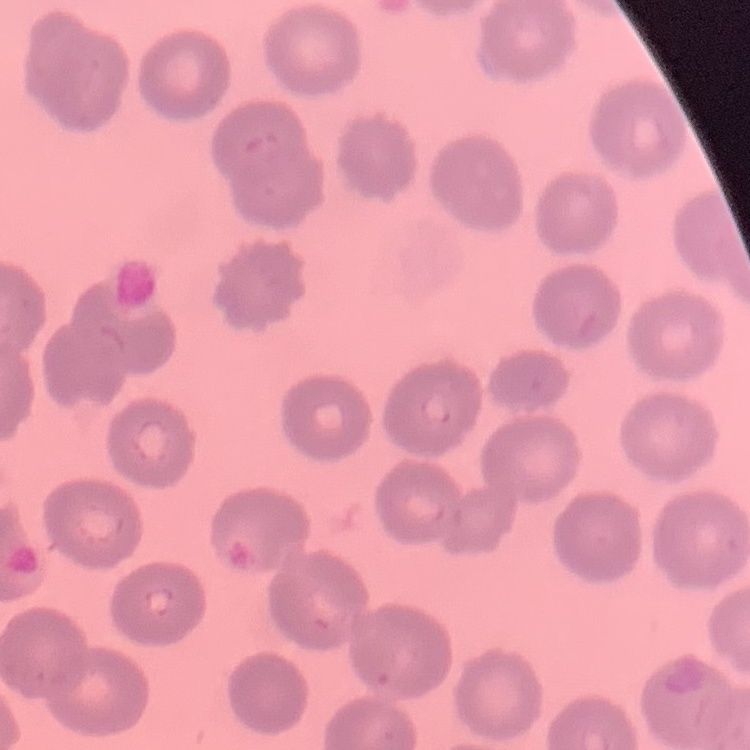

The erythrocytes exhibit no rouleaux formation. Field's or Giemsa stain. Square crop of a larger photomicrograph. Thin blood smear.